Comment on the morphology of the erythrocytes.
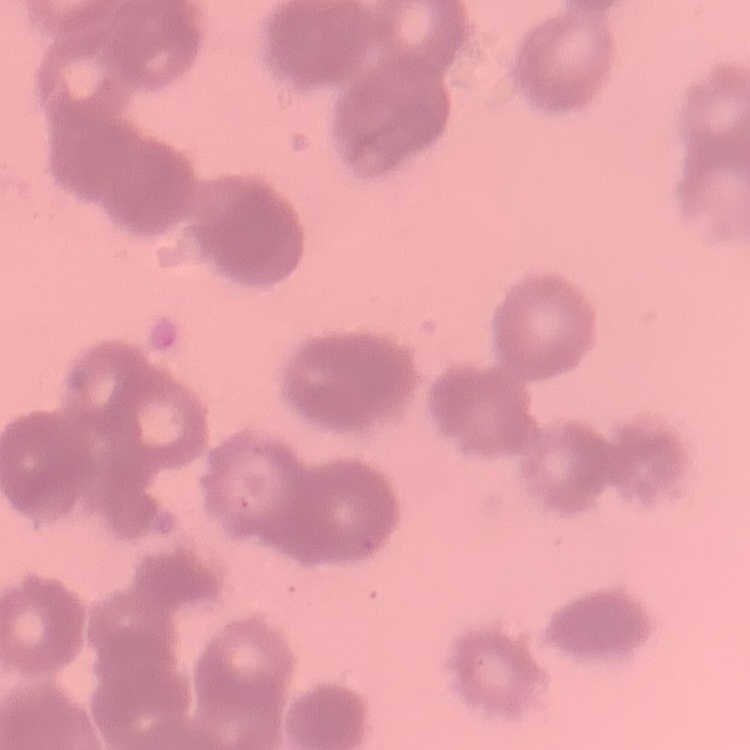
They show rouleaux formation.

Thin blood smear. One tile cut from a larger photomicrograph. Field's or Giemsa stain.